Name the cell type shown.
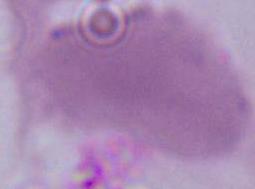
An erythrocyte.

Micrograph. 1000x magnification.